Describe the morphology of the erythrocytes.
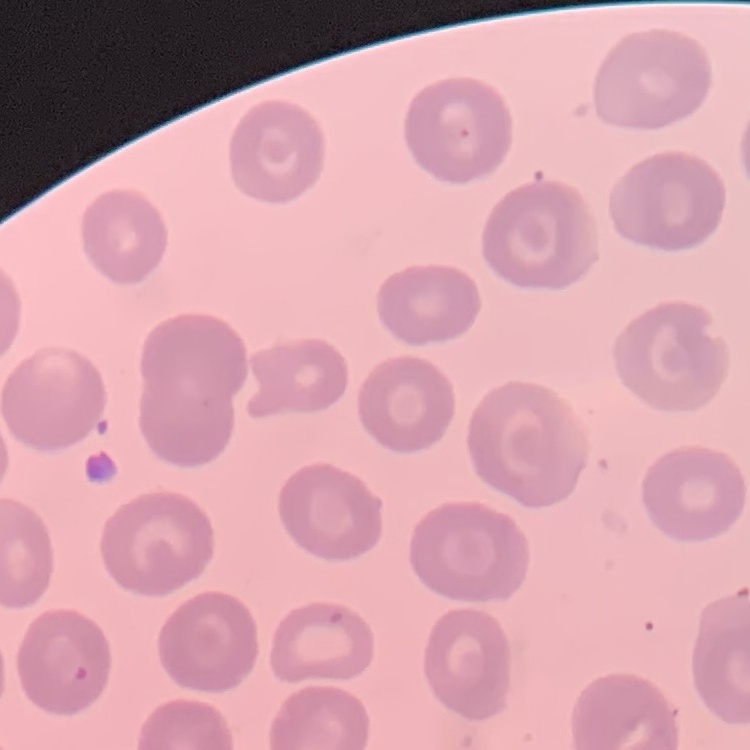
They show no rouleaux formation.

stain = Field's or Giemsa
image type = square crop of a larger photomicrograph
preparation = thin blood film